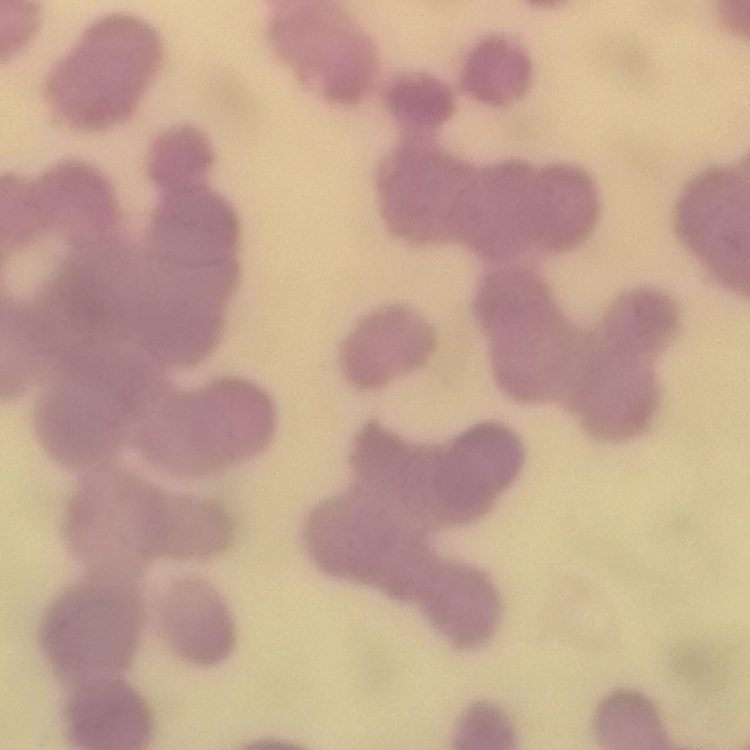
Summary:
  - Erythrocyte morphology: rouleaux formation
  - Preparation: thin blood film
  - Stain: Field's or Giemsa
  - Image type: square crop of a larger photomicrograph